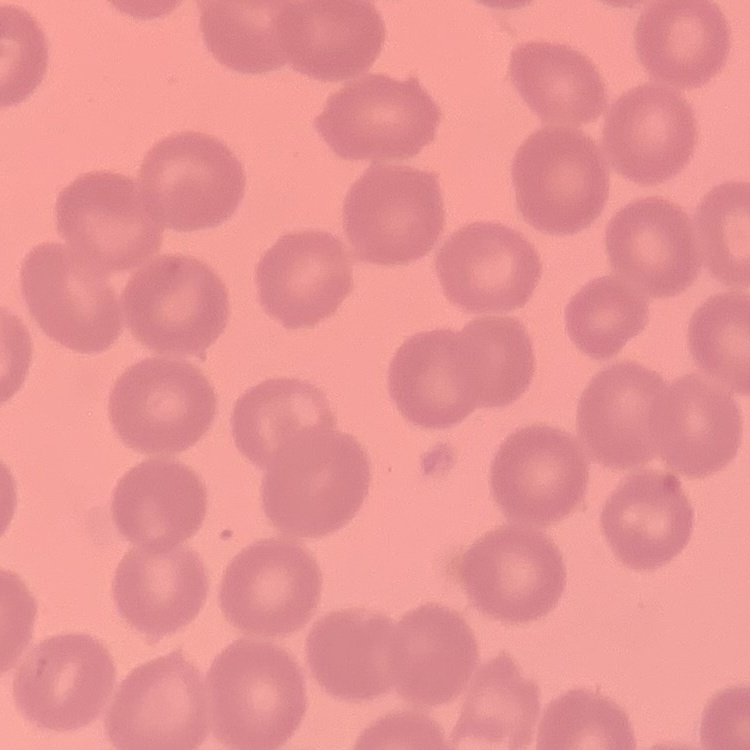
{
  "erythrocyte_morphology": "no rouleaux formation",
  "image_type": "square crop of a larger photomicrograph",
  "stain": "Field's or Giemsa",
  "preparation": "thin peripheral smear"
}